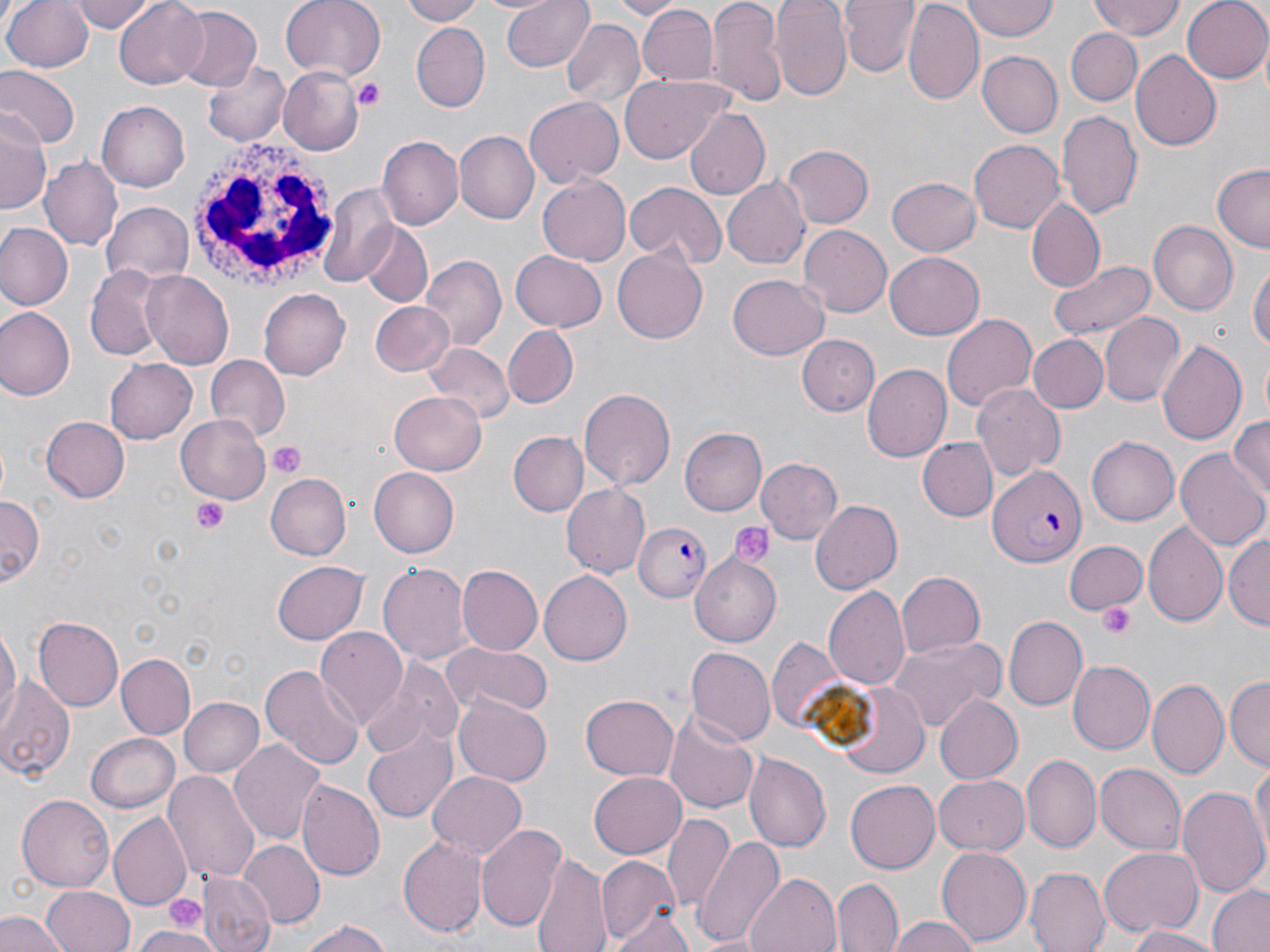

Summary:
  - Coordinate format: approximate bounding boxes as named x1/y1/x2/y2 corners in pixels
  - Plasmodium falciparum-infected red blood cell locations: (x1=989, y1=465, x2=1085, y2=570), (x1=634, y1=521, x2=710, y2=602)
  - Uninfected red blood cell locations: (x1=3, y1=0, x2=94, y2=73), (x1=72, y1=0, x2=157, y2=32), (x1=113, y1=0, x2=210, y2=89), (x1=280, y1=0, x2=385, y2=82), (x1=396, y1=0, x2=485, y2=25), (x1=501, y1=0, x2=595, y2=72), (x1=613, y1=0, x2=678, y2=18), (x1=773, y1=0, x2=851, y2=100), (x1=840, y1=0, x2=921, y2=77), (x1=963, y1=0, x2=1056, y2=40), (x1=1089, y1=0, x2=1184, y2=40), (x1=1182, y1=0, x2=1270, y2=84), (x1=708, y1=1, x2=786, y2=105), (x1=903, y1=2, x2=984, y2=108), (x1=635, y1=4, x2=717, y2=88), (x1=169, y1=7, x2=260, y2=92), (x1=560, y1=19, x2=644, y2=109), (x1=411, y1=24, x2=489, y2=111), (x1=1065, y1=27, x2=1142, y2=107), (x1=1131, y1=49, x2=1225, y2=149), (x1=977, y1=51, x2=1062, y2=138), (x1=200, y1=59, x2=291, y2=149), (x1=0, y1=66, x2=79, y2=151), (x1=280, y1=68, x2=361, y2=152), (x1=619, y1=72, x2=730, y2=163), (x1=524, y1=96, x2=623, y2=187), (x1=98, y1=100, x2=192, y2=193), (x1=683, y1=108, x2=770, y2=202), (x1=0, y1=110, x2=50, y2=215), (x1=1056, y1=110, x2=1143, y2=222), (x1=456, y1=131, x2=539, y2=223), (x1=377, y1=136, x2=463, y2=229), (x1=969, y1=139, x2=1066, y2=233), (x1=783, y1=145, x2=873, y2=228), (x1=41, y1=157, x2=120, y2=247), (x1=1211, y1=165, x2=1270, y2=251), (x1=538, y1=173, x2=630, y2=265), (x1=888, y1=176, x2=982, y2=257), (x1=724, y1=179, x2=810, y2=269), (x1=624, y1=183, x2=725, y2=269), (x1=318, y1=184, x2=398, y2=287), (x1=1028, y1=198, x2=1106, y2=293), (x1=102, y1=203, x2=193, y2=285), (x1=1149, y1=221, x2=1238, y2=313), (x1=0, y1=222, x2=73, y2=309), (x1=358, y1=224, x2=432, y2=306), (x1=799, y1=225, x2=891, y2=317), (x1=611, y1=249, x2=708, y2=344), (x1=512, y1=250, x2=607, y2=330), (x1=884, y1=251, x2=985, y2=340), (x1=420, y1=256, x2=505, y2=350), (x1=1048, y1=259, x2=1156, y2=342), (x1=1249, y1=261, x2=1269, y2=360), (x1=84, y1=266, x2=164, y2=359), (x1=141, y1=268, x2=235, y2=367), (x1=728, y1=274, x2=831, y2=361), (x1=260, y1=290, x2=350, y2=379), (x1=367, y1=300, x2=455, y2=377), (x1=2, y1=308, x2=74, y2=400), (x1=942, y1=312, x2=1036, y2=413), (x1=1100, y1=312, x2=1184, y2=406), (x1=504, y1=325, x2=577, y2=407), (x1=1030, y1=334, x2=1106, y2=413), (x1=798, y1=335, x2=879, y2=416), (x1=1156, y1=338, x2=1247, y2=448), (x1=423, y1=344, x2=511, y2=427), (x1=104, y1=355, x2=198, y2=443), (x1=203, y1=356, x2=289, y2=442), (x1=863, y1=363, x2=952, y2=461), (x1=972, y1=383, x2=1064, y2=480), (x1=578, y1=387, x2=676, y2=489), (x1=380, y1=390, x2=473, y2=555), (x1=388, y1=393, x2=486, y2=475), (x1=1227, y1=414, x2=1270, y2=501), (x1=176, y1=415, x2=269, y2=501), (x1=40, y1=416, x2=130, y2=504), (x1=679, y1=428, x2=766, y2=517), (x1=507, y1=432, x2=589, y2=516), (x1=1088, y1=437, x2=1179, y2=526), (x1=920, y1=439, x2=995, y2=521), (x1=1175, y1=448, x2=1270, y2=552), (x1=756, y1=458, x2=843, y2=544), (x1=370, y1=465, x2=463, y2=558), (x1=265, y1=472, x2=352, y2=561), (x1=561, y1=483, x2=650, y2=578), (x1=0, y1=495, x2=44, y2=588), (x1=811, y1=500, x2=905, y2=595), (x1=1145, y1=520, x2=1226, y2=627), (x1=1227, y1=536, x2=1269, y2=631), (x1=1063, y1=541, x2=1147, y2=613), (x1=689, y1=553, x2=782, y2=648), (x1=379, y1=560, x2=472, y2=669), (x1=271, y1=561, x2=369, y2=646), (x1=456, y1=566, x2=542, y2=657), (x1=539, y1=572, x2=631, y2=663), (x1=896, y1=572, x2=987, y2=659), (x1=824, y1=585, x2=909, y2=691), (x1=1004, y1=615, x2=1087, y2=711), (x1=33, y1=617, x2=124, y2=709), (x1=0, y1=620, x2=19, y2=731), (x1=315, y1=628, x2=407, y2=731), (x1=768, y1=635, x2=860, y2=740), (x1=887, y1=636, x2=1002, y2=731), (x1=443, y1=644, x2=550, y2=716), (x1=684, y1=646, x2=774, y2=744), (x1=116, y1=653, x2=195, y2=738), (x1=359, y1=658, x2=462, y2=756), (x1=1069, y1=659, x2=1158, y2=753), (x1=261, y1=662, x2=364, y2=770), (x1=0, y1=674, x2=77, y2=781), (x1=1226, y1=677, x2=1269, y2=770), (x1=1148, y1=679, x2=1227, y2=778), (x1=836, y1=681, x2=930, y2=778), (x1=581, y1=694, x2=678, y2=780), (x1=933, y1=694, x2=1023, y2=785), (x1=453, y1=695, x2=553, y2=785), (x1=177, y1=696, x2=263, y2=779), (x1=663, y1=711, x2=760, y2=814), (x1=361, y1=731, x2=457, y2=823), (x1=86, y1=732, x2=181, y2=813), (x1=229, y1=735, x2=326, y2=844), (x1=744, y1=753, x2=831, y2=854), (x1=1022, y1=754, x2=1101, y2=852), (x1=1250, y1=758, x2=1269, y2=862), (x1=1096, y1=764, x2=1187, y2=854), (x1=162, y1=769, x2=259, y2=886), (x1=589, y1=769, x2=687, y2=858), (x1=427, y1=770, x2=527, y2=860), (x1=933, y1=775, x2=1030, y2=855), (x1=845, y1=779, x2=941, y2=873), (x1=297, y1=782, x2=384, y2=881), (x1=1175, y1=784, x2=1269, y2=896), (x1=17, y1=796, x2=115, y2=891), (x1=108, y1=811, x2=191, y2=910), (x1=660, y1=814, x2=735, y2=913), (x1=478, y1=823, x2=567, y2=935), (x1=397, y1=833, x2=487, y2=938), (x1=692, y1=834, x2=785, y2=948), (x1=238, y1=841, x2=324, y2=929), (x1=937, y1=845, x2=1035, y2=944), (x1=1100, y1=849, x2=1202, y2=937), (x1=534, y1=852, x2=610, y2=952), (x1=598, y1=855, x2=682, y2=945), (x1=1026, y1=867, x2=1111, y2=952), (x1=746, y1=873, x2=841, y2=952), (x1=199, y1=874, x2=274, y2=952), (x1=833, y1=878, x2=902, y2=952), (x1=1205, y1=882, x2=1270, y2=952), (x1=43, y1=884, x2=133, y2=952), (x1=609, y1=907, x2=696, y2=950), (x1=0, y1=910, x2=67, y2=952), (x1=887, y1=914, x2=982, y2=952), (x1=298, y1=918, x2=392, y2=952), (x1=1125, y1=923, x2=1221, y2=952), (x1=129, y1=927, x2=228, y2=952)
  - Platelet locations: (x1=354, y1=78, x2=386, y2=111), (x1=268, y1=442, x2=304, y2=479), (x1=193, y1=496, x2=230, y2=534), (x1=730, y1=521, x2=776, y2=571), (x1=1099, y1=602, x2=1138, y2=639), (x1=165, y1=895, x2=204, y2=929)
  - White blood cell locations: (x1=188, y1=135, x2=337, y2=291)
  - Slide-level diagnosis: Plasmodium falciparum
  - Image size: 1270×952 pixels
  - Preparation: thin blood film
  - Modality: light microscopy
  - Magnification: 1000x
  - Stain: May-Grünwald-Giemsa
  - Field of view: one of a larger specimen